Point out each leukocyte.
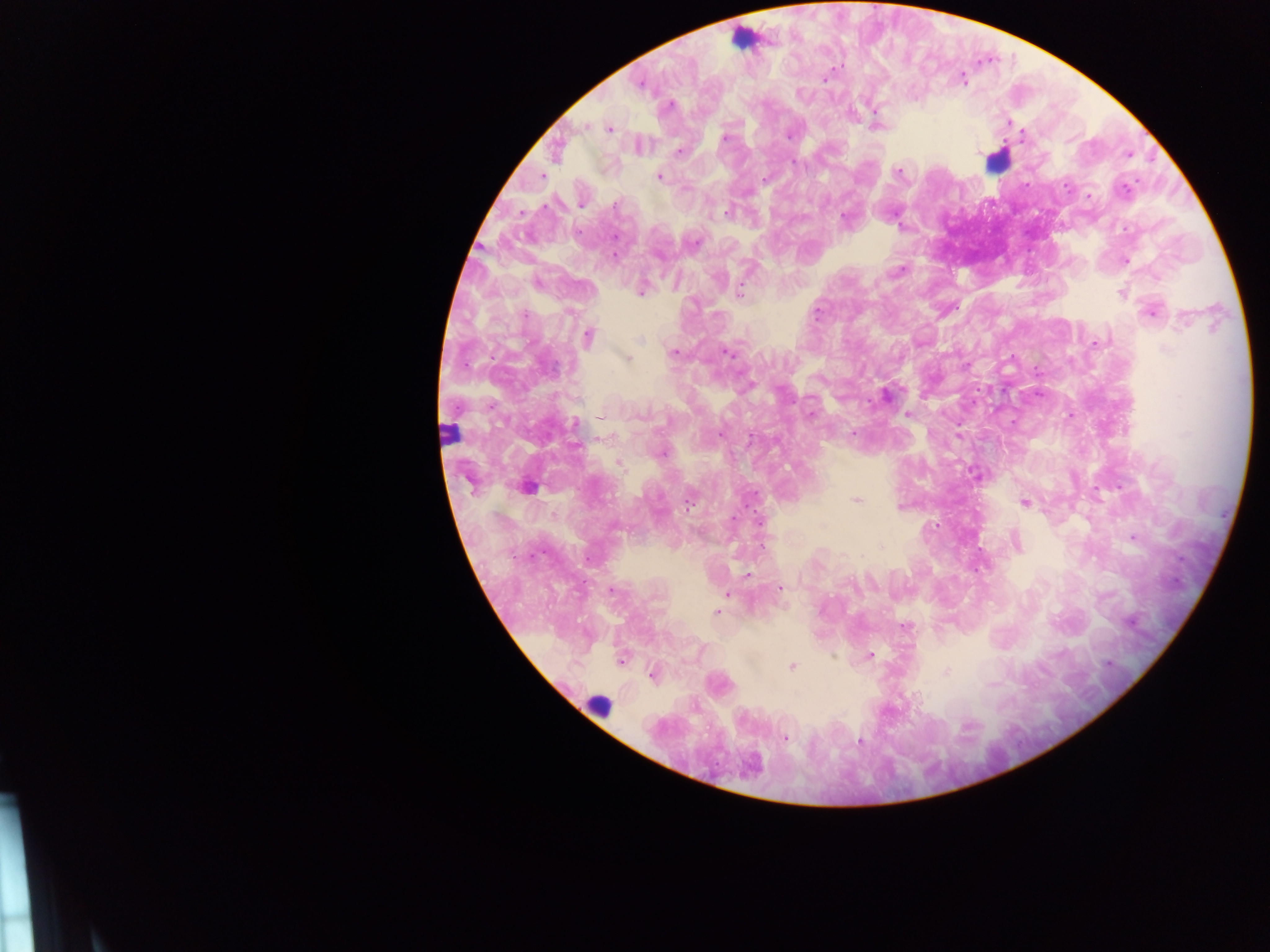

Approximate centers as (x, y) in pixels.
Leukocytes: (743, 39), (996, 161), (448, 433), (600, 705).

preparation = thick blood smear
country = Ghana
capture = mobile-phone photograph through a microscope
image size = 1270×952 pixels
field of view = single
Plasmodium parasite locations = approximate centers as (x, y) in pixels: (824, 78), (961, 79), (640, 83), (670, 105), (1008, 122), (584, 126), (875, 126), (609, 129), (790, 133), (724, 138), (639, 146), (556, 150), (679, 151), (1128, 155), (897, 171), (659, 176), (766, 179), (1088, 195), (582, 203), (726, 211), (845, 220), (1125, 261), (902, 268), (642, 288), (739, 293), (1122, 293), (1152, 309), (588, 336), (1094, 343), (726, 351), (673, 352), (626, 358), (885, 396), (809, 415), (907, 415), (601, 416), (1068, 416), (574, 424), (854, 432), (619, 463), (976, 474), (526, 487), (689, 498), (856, 500), (1024, 503), (1133, 537), (1015, 541), (978, 562), (746, 575), (781, 588), (611, 590), (727, 593), (715, 612), (905, 627), (869, 655), (621, 659), (791, 666), (947, 671), (652, 674), (784, 738), (859, 740)